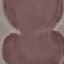
malaria_status: uninfected
image_type: cell patch, automatically extracted from a larger field of view and resized to 64 × 64 pixels
capture: smartphone through the microscope eyepiece
preparation: thin blood smear
stain: Giemsa